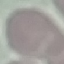

Result: no malaria parasites detected. Photographed with a smartphone camera at the microscope eyepiece. Thin smear of blood. Giemsa-stained preparation. Cell patch, automatically extracted from a larger field of view and resized to 64 × 64 pixels.